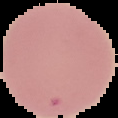
Summary:
  - Image size: 118×118 pixels
  - Malaria status: uninfected
  - Preparation: thin blood film
  - Image type: segmented cell region on a black background